Classify this cell by malaria status.
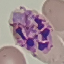

Parasitized.

image type = automatically extracted cell patch, resized to 64 × 64 pixels
preparation = thin blood film
stain = Giemsa
capture = smartphone camera at the microscope eyepiece